Report the malaria status of this cell.
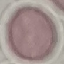
Uninfected.

capture: smartphone through the microscope eyepiece
stain: Giemsa
preparation: thin smear
image_type: cell patch, automatically extracted from a larger field of view and resized to 64 × 64 pixels